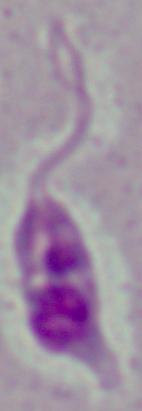

identification = Leishmania
magnification = 1000x
modality = photomicrograph